Outline each Plasmodium ovale-infected red blood cell.
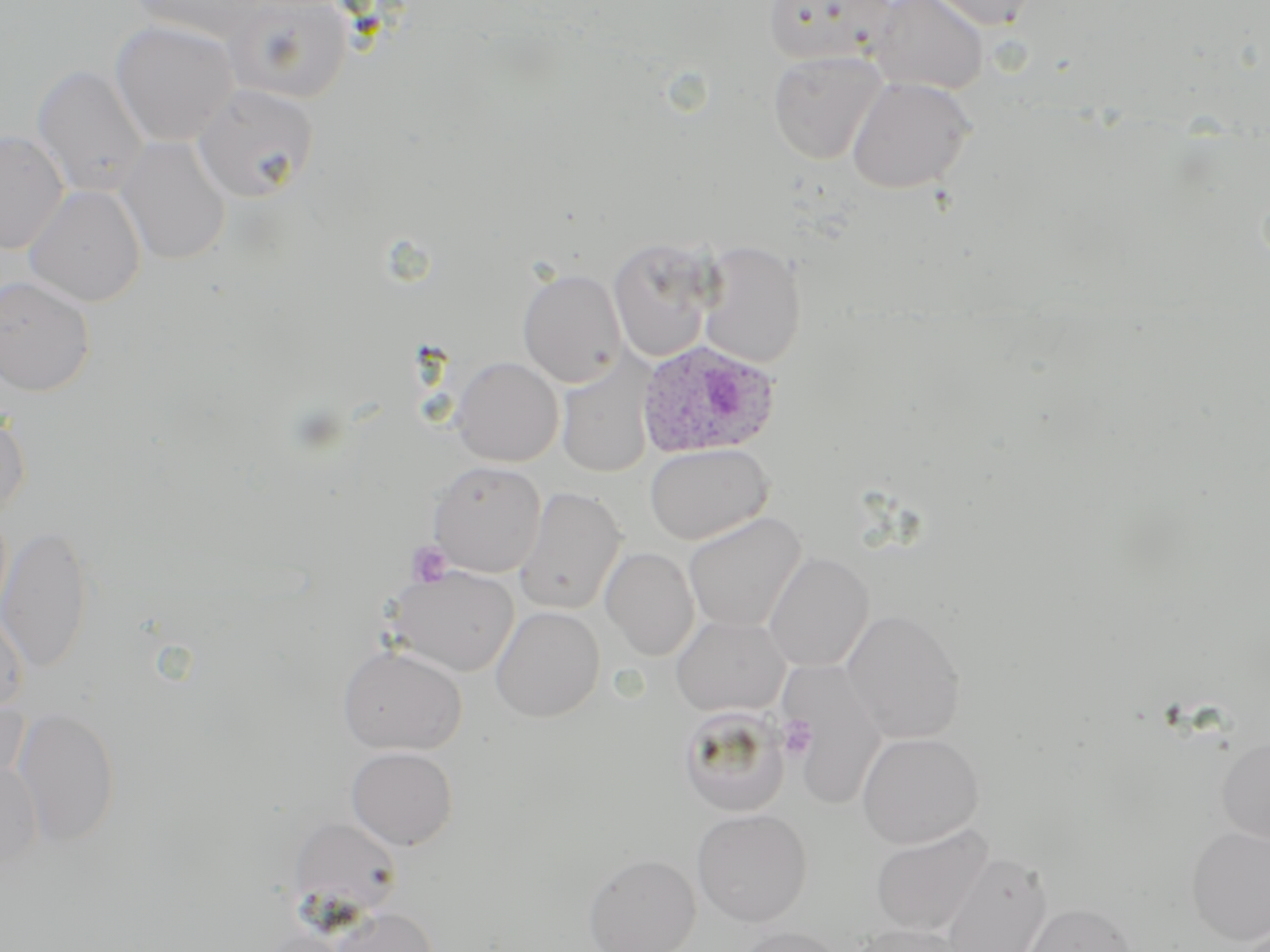
Approximate bounding boxes as (x1,y1)-(x2,y2) corner pairs in pixels.
Plasmodium ovale-infected red blood cells: (636,339)-(781,459).

slide_level_diagnosis: Plasmodium ovale
image_size: 1270×952 pixels
stain: May-Grünwald-Giemsa
magnification: 1000x
platelet_locations: 'approximate bounding boxes as (x1,y1)-(x2,y2) corner pairs in pixels: (406,541)-(453,588), (779,716)-(816,760)'
field_of_view: one of a larger specimen
modality: light microscopy
uninfected_red_blood_cell_locations: 'approximate bounding boxes as (x1,y1)-(x2,y2) corner pairs in pixels: (128,0)-(268,41), (223,0)-(353,104), (761,0)-(898,67), (867,0)-(989,94), (925,0)-(1042,30), (110,20)-(239,147), (767,50)-(888,165), (32,64)-(149,196), (847,76)-(975,194), (194,83)-(319,202), (0,129)-(69,254), (116,136)-(232,265), (24,184)-(147,307), (608,239)-(717,362), (696,241)-(807,368), (517,268)-(627,387), (0,275)-(96,397), (451,357)-(563,467), (557,357)-(655,479), (0,409)-(31,517), (644,443)-(772,544), (428,460)-(546,577), (514,487)-(626,615), (501,490)-(613,726), (683,512)-(806,632), (0,525)-(94,674), (601,547)-(699,660), (764,552)-(874,671), (388,565)-(519,677), (0,603)-(29,717), (491,606)-(605,722), (843,609)-(965,743), (672,616)-(789,716), (338,646)-(467,755), (781,659)-(888,812), (0,692)-(30,793), (678,706)-(790,816), (12,707)-(122,847), (857,732)-(984,848), (1215,734)-(1270,846), (346,746)-(458,850), (0,759)-(43,870), (692,808)-(812,926), (287,816)-(404,920), (870,824)-(994,937), (1187,824)-(1270,945), (939,852)-(1051,952), (583,853)-(700,952), (1022,901)-(1137,952), (331,906)-(439,952), (850,924)-(968,952), (731,926)-(849,952)'
preparation: thin blood smear